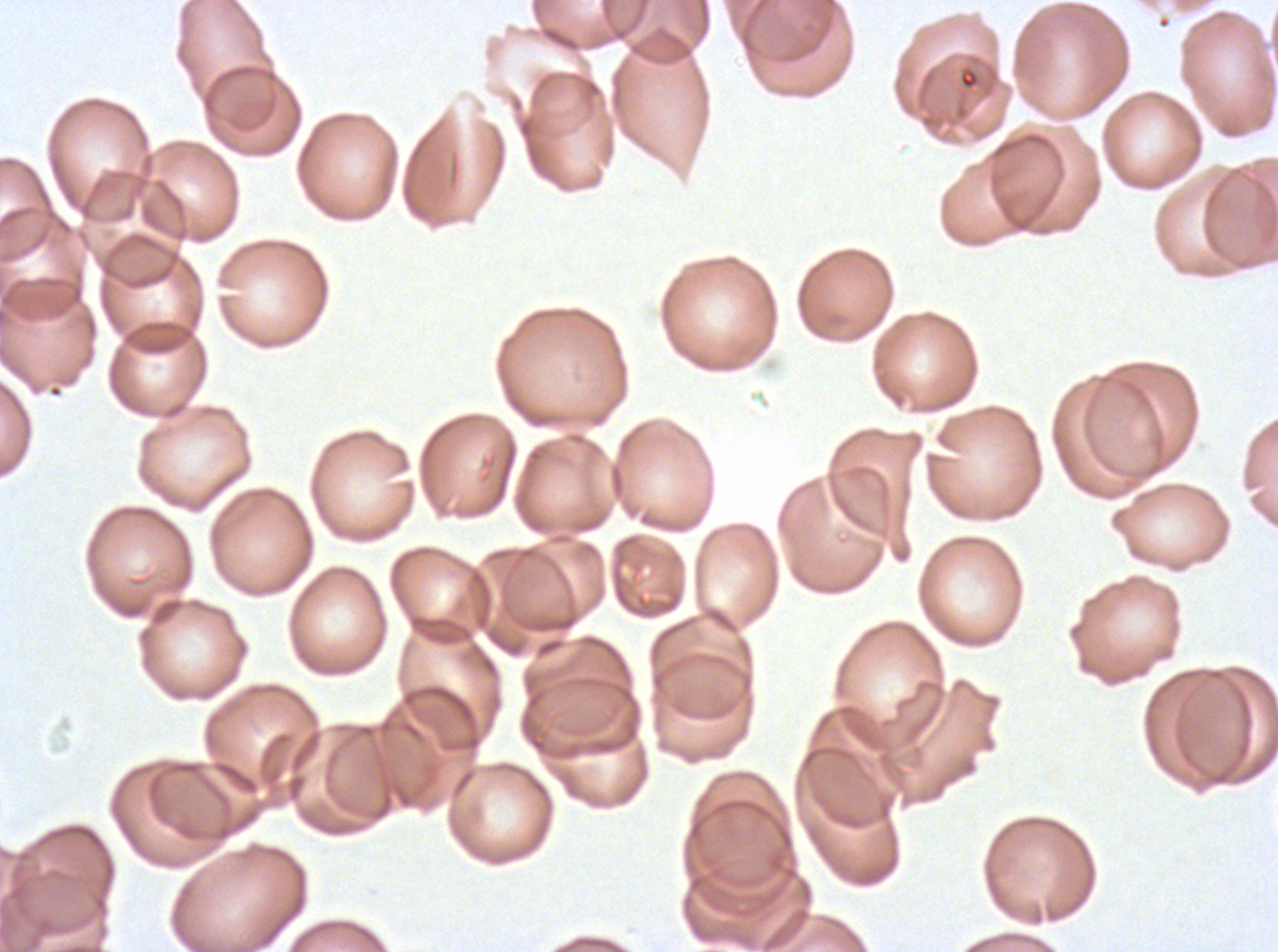

Approximate bounding boxes as [x1, y1, x2, y2] in pixels. Debris locations: [958, 68, 980, 91]. Thin blood smear. A sub-image separated from a larger composite. Giemsa stain. P. falciparum from a patient in The Gambia, cultured ex vivo for 24 to 48 hours. Image is 1278×952 pixels.